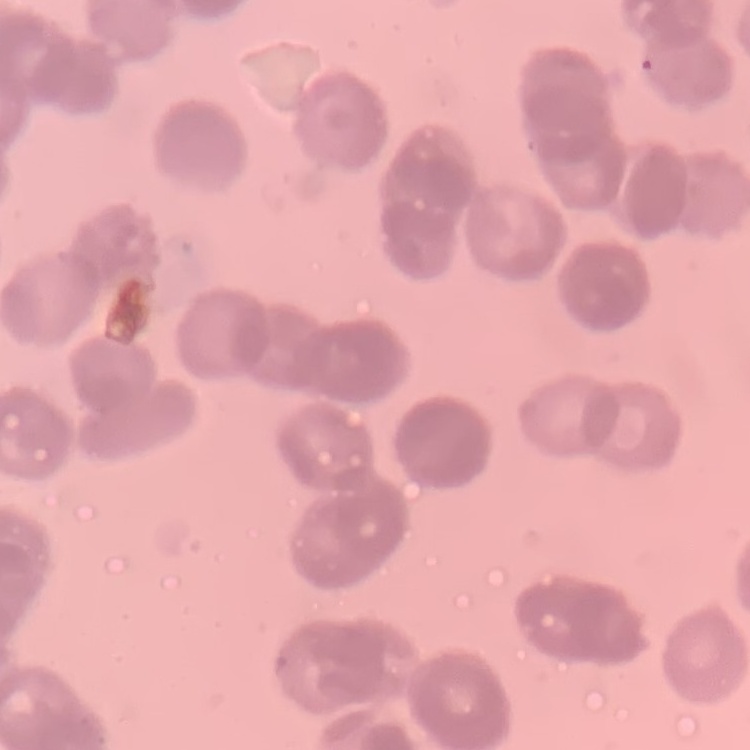

Summary:
  - Red blood cell morphology: rouleaux formation
  - Image type: square crop of a larger photomicrograph
  - Stain: Field's or Giemsa
  - Preparation: thin peripheral smear